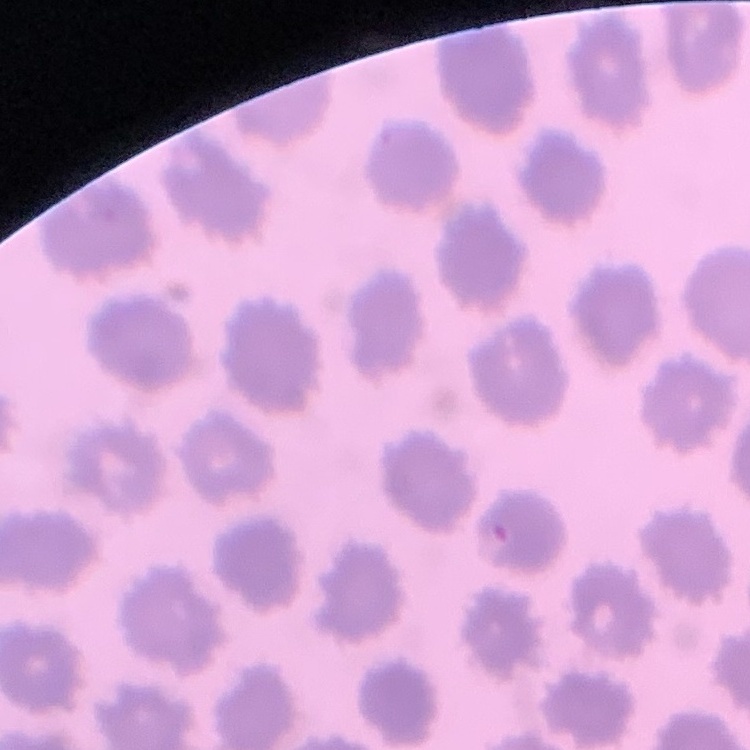

{
  "erythrocyte_morphology": "no rouleaux formation",
  "image_type": "one tile cut from a larger photomicrograph",
  "stain": "Field's or Giemsa",
  "preparation": "thin peripheral smear"
}